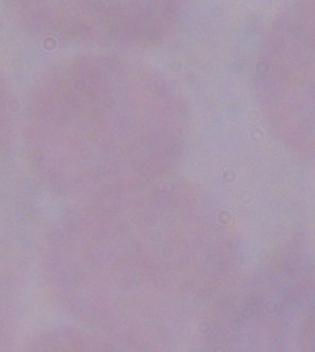

magnification = 1000x
modality = micrograph
identification = trypanosome